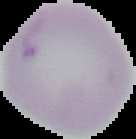
image size = 136×139 pixels
malaria status = uninfected
preparation = thin blood film
image type = segmented cell region on a black background